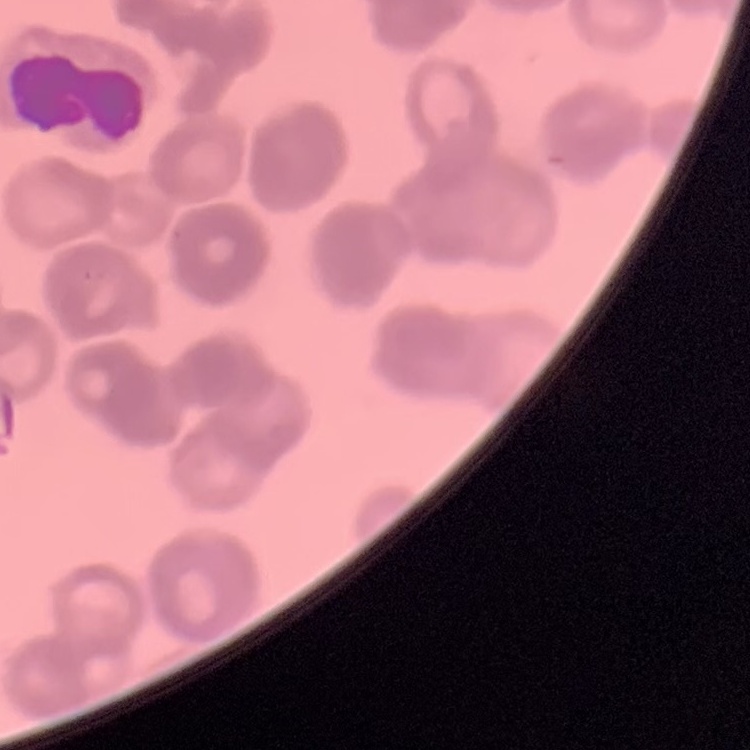

Summary:
  - Red blood cell morphology: rouleaux formation
  - Stain: Field's or Giemsa
  - Image type: square crop of a larger photomicrograph
  - Preparation: thin blood film